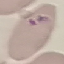
Summary:
  - Malaria status: parasitized
  - Stain: Giemsa
  - Preparation: thin smear
  - Image type: automatically extracted cell patch, resized to 64 × 64 pixels
  - Capture: smartphone camera at the microscope eyepiece